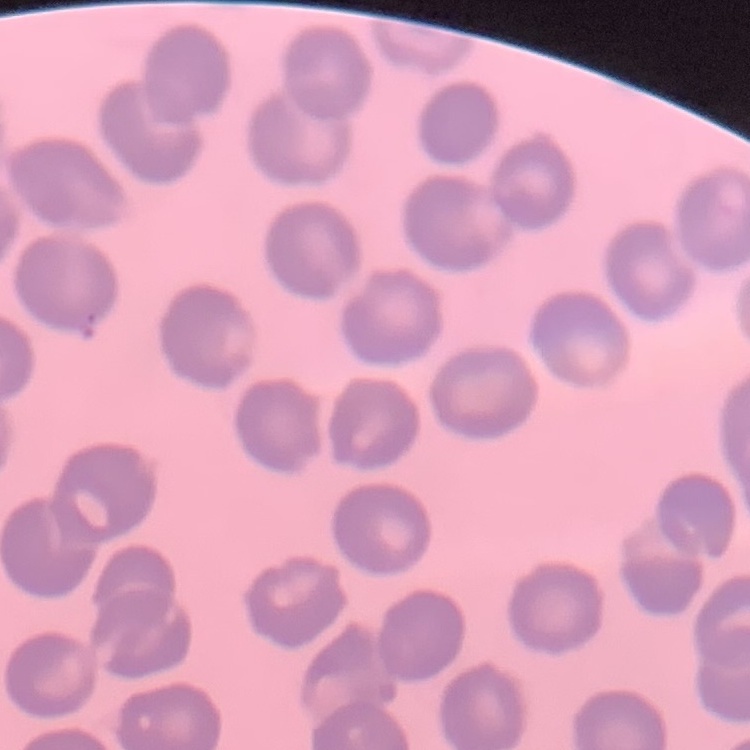

The red blood cells show no rouleaux formation. Square crop of a larger photomicrograph. Thin peripheral smear. Field's or Giemsa stain.